Name the blood parasite species.
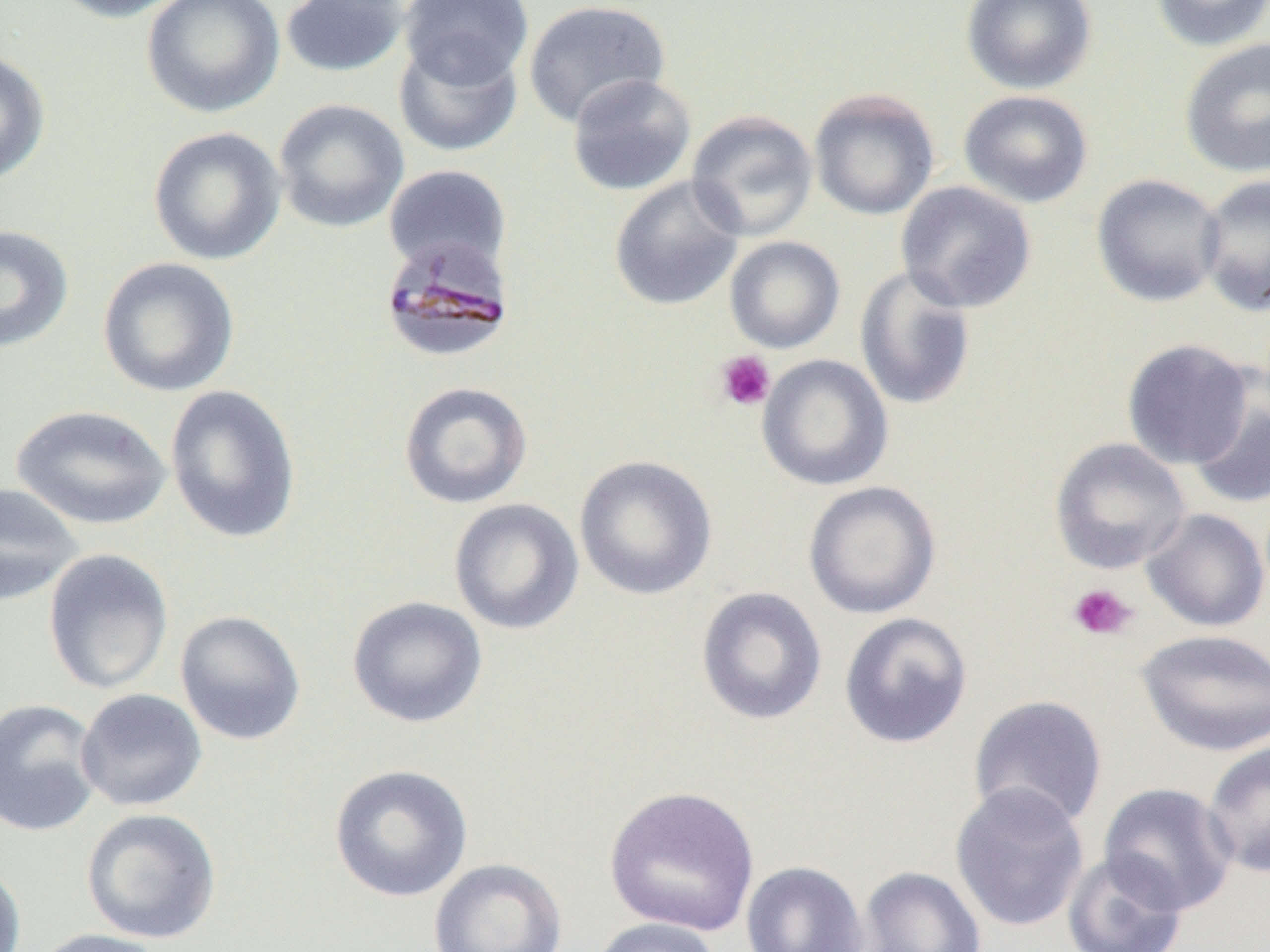
Plasmodium malariae.

preparation = thin blood smear
uninfected red blood cell locations = approximate bounding boxes as (x1,y1)-(x2,y2) corner pairs in pixels: (46,0)-(190,22), (141,0)-(284,118), (280,0)-(410,77), (400,0)-(532,88), (960,0)-(1098,94), (1150,0)-(1270,52), (522,1)-(671,127), (1179,37)-(1270,178), (393,39)-(523,157), (0,49)-(51,185), (565,73)-(697,196), (808,88)-(940,221), (957,89)-(1094,209), (273,98)-(409,233), (686,109)-(819,242), (148,126)-(287,265), (384,164)-(512,275), (1091,173)-(1227,307), (1197,174)-(1270,317), (608,175)-(746,311), (895,181)-(1037,313), (0,224)-(75,353), (724,236)-(845,353), (97,257)-(240,397), (853,265)-(977,411), (1121,338)-(1254,470), (757,354)-(894,491), (1188,366)-(1270,511), (398,381)-(533,509), (164,384)-(302,545), (12,404)-(172,530), (1049,437)-(1191,574), (574,455)-(718,600), (802,480)-(942,619), (0,481)-(84,607), (448,497)-(584,635), (1140,508)-(1269,632), (42,548)-(174,695), (696,586)-(827,726), (346,595)-(488,728), (174,609)-(307,746), (838,611)-(974,749), (1135,628)-(1270,756), (76,688)-(208,812), (968,694)-(1108,829), (0,698)-(104,837), (1202,739)-(1270,878), (329,764)-(473,902), (949,782)-(1090,933), (1098,782)-(1239,916), (603,785)-(760,937), (81,807)-(222,944), (1062,850)-(1189,952), (0,858)-(26,952), (428,858)-(568,952), (740,860)-(869,952), (856,865)-(987,952), (589,917)-(725,952), (29,928)-(170,952)
field of view = one of a larger specimen
image size = 1270×952 pixels
platelet locations = approximate bounding boxes as (x1,y1)-(x2,y2) corner pairs in pixels: (714,350)-(776,411), (1067,582)-(1137,641)
modality = optical microscopy
magnification = 1000x
Plasmodium malariae-infected red blood cell locations = approximate bounding boxes as (x1,y1)-(x2,y2) corner pairs in pixels: (379,237)-(516,364)